Classify this cell by malaria status.
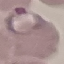

Parasitized.

image type = automatically extracted cell patch, resized to 64 × 64 pixels
preparation = thin blood film
capture = smartphone camera at the microscope eyepiece
stain = Giemsa